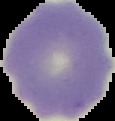

{
  "malaria_status": "uninfected",
  "image_size": "115×121 pixels",
  "preparation": "thin blood film",
  "image_type": "segmented cell region with the area outside set to black"
}